Mark where cells are.
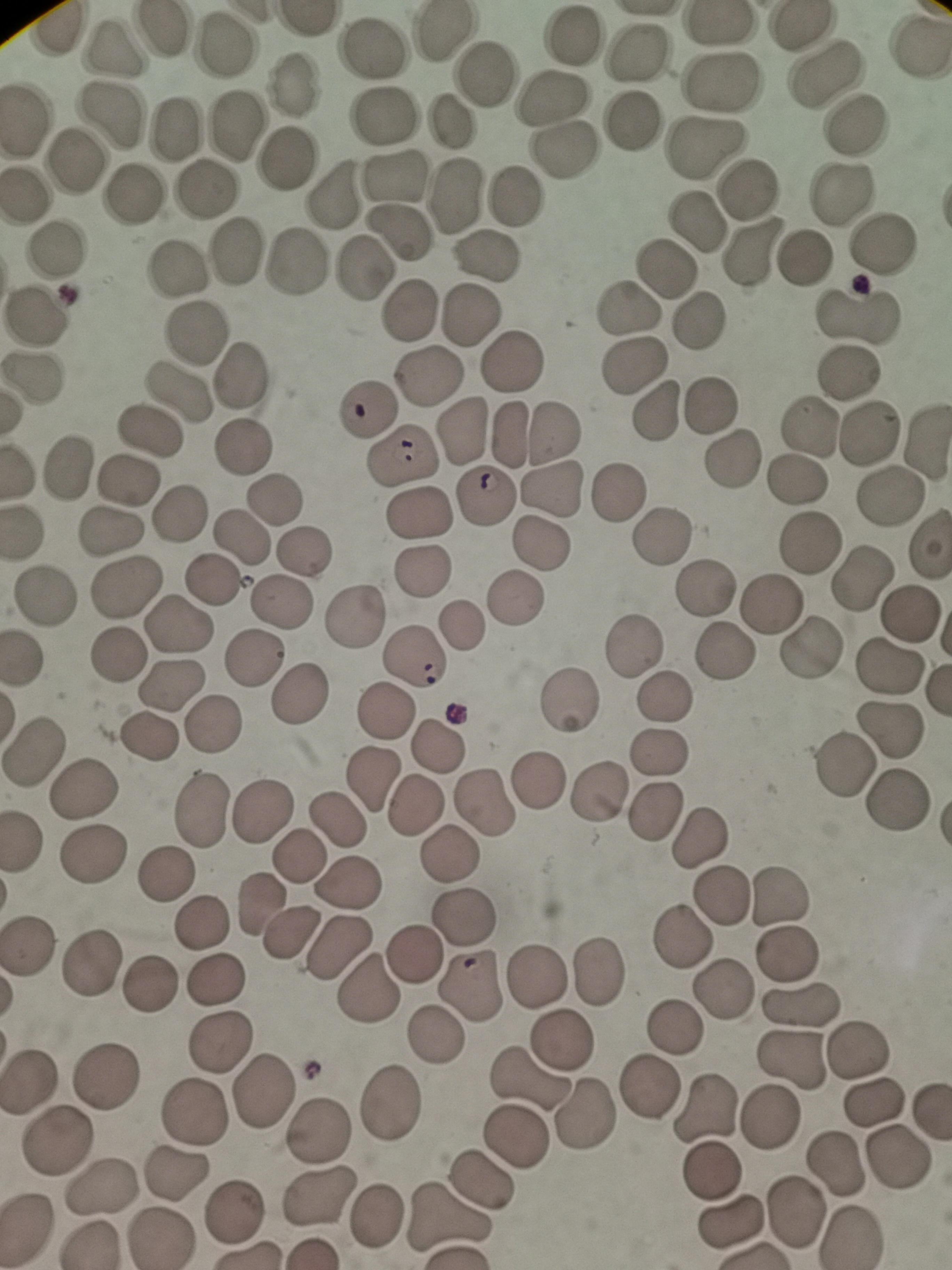
Approximate centers as (x, y) in pixels.
Cells: (159, 32), (572, 35), (918, 46), (222, 48), (112, 50), (370, 51), (633, 53), (824, 68), (485, 73), (718, 79), (291, 85), (551, 99), (386, 116), (108, 118), (450, 121), (631, 122), (855, 122), (238, 124), (174, 129), (705, 145), (566, 150), (75, 159), (289, 159), (395, 175), (747, 184), (205, 189), (131, 190), (27, 192), (461, 193), (844, 193), (332, 194), (516, 195), (698, 222), (398, 238), (883, 242), (57, 245), (236, 252), (756, 252), (484, 258), (804, 258), (181, 265), (666, 265), (298, 267), (361, 269), (412, 307), (632, 308), (856, 309), (473, 314), (36, 318), (700, 320), (197, 331), (516, 357), (637, 368), (848, 374), (241, 375), (425, 375), (37, 379), (179, 392), (709, 406), (365, 407), (656, 412), (809, 427), (875, 429), (556, 430), (149, 431), (464, 431), (510, 434), (926, 440), (243, 446), (404, 456), (734, 459), (68, 468), (128, 477), (797, 481), (551, 493), (615, 493), (886, 496), (484, 498), (277, 500), (177, 510), (415, 513), (106, 533), (665, 534), (242, 538), (927, 539), (809, 542), (538, 546), (304, 550), (421, 569), (859, 574), (213, 581), (702, 584), (128, 585), (45, 598), (285, 601), (515, 601), (772, 608), (910, 612), (357, 614), (179, 623), (462, 627), (812, 643), (635, 644), (116, 655), (413, 655), (254, 657), (890, 668), (174, 683), (298, 697), (665, 701), (570, 702), (385, 710), (213, 725), (889, 728), (150, 738), (441, 743), (32, 748), (656, 752), (843, 762), (536, 778), (372, 781), (84, 788), (599, 790), (485, 798), (900, 801), (655, 811), (264, 813), (201, 814), (338, 820), (700, 835), (93, 851), (446, 853), (298, 858), (163, 877), (348, 885), (783, 893), (721, 898), (259, 905), (464, 914), (202, 922), (287, 934), (681, 936), (31, 946), (339, 946), (786, 953), (414, 954), (91, 963), (597, 972), (216, 976), (537, 976), (725, 985), (151, 988), (366, 989), (468, 991), (798, 997), (675, 1027), (436, 1037), (562, 1041), (215, 1042), (860, 1051), (792, 1062), (107, 1078), (526, 1078), (28, 1084), (265, 1089), (647, 1091), (707, 1102), (878, 1102), (391, 1106), (197, 1114), (586, 1119), (767, 1120), (319, 1131), (517, 1139), (56, 1143), (895, 1158), (837, 1167), (709, 1169), (174, 1176), (479, 1182), (103, 1188), (319, 1198), (235, 1212), (374, 1214), (795, 1215), (447, 1221), (728, 1221), (854, 1237), (159, 1239).

Image is 952×1270 pixels. Thin blood film. Single field of view. Giemsa-stained preparation. Photographed with a smartphone camera at the microscope eyepiece.